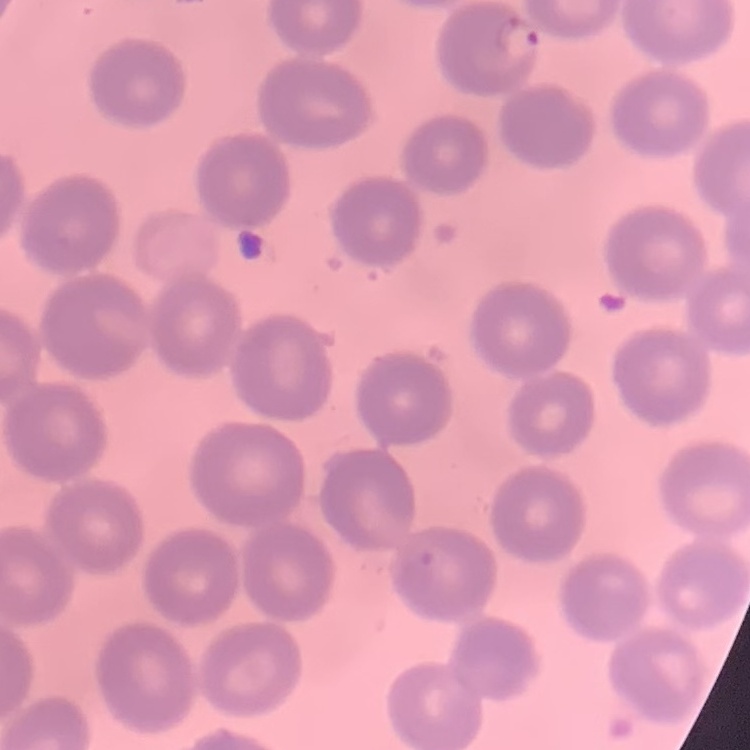

Summary:
  - Erythrocyte morphology: no rouleaux formation
  - Image type: one tile cut from a larger photomicrograph
  - Stain: Field's or Giemsa
  - Preparation: thin blood smear